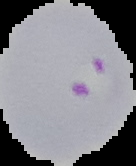
Result: Plasmodium parasites identified. Image is 136×166 pixels. Cell region segmented out of the field of view; the surrounding area is masked to black. From a thin blood smear.